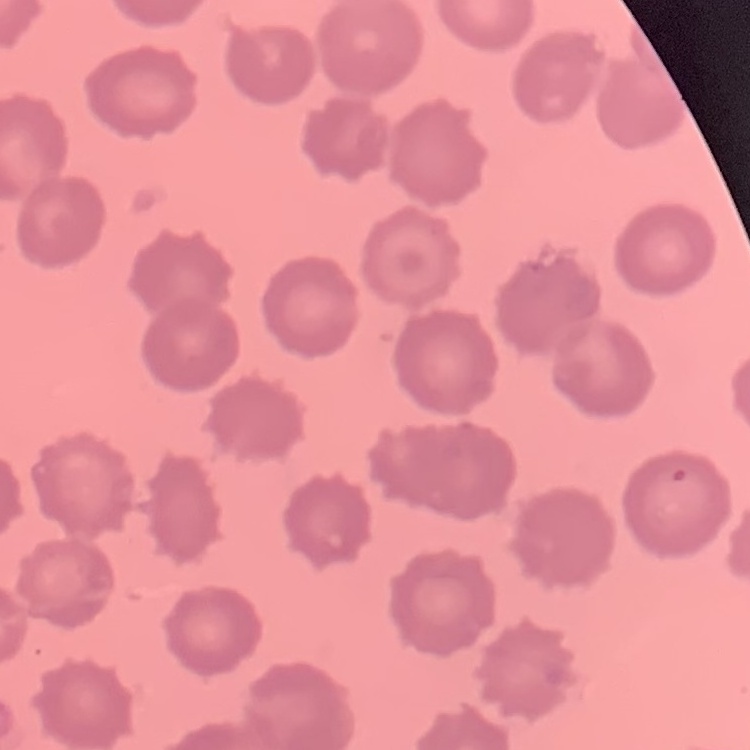
The erythrocytes exhibit no rouleaux formation. Field's or Giemsa stain. Thin blood smear. One tile cut from a larger photomicrograph.